Give the extent of all Trypanosoma brucei.
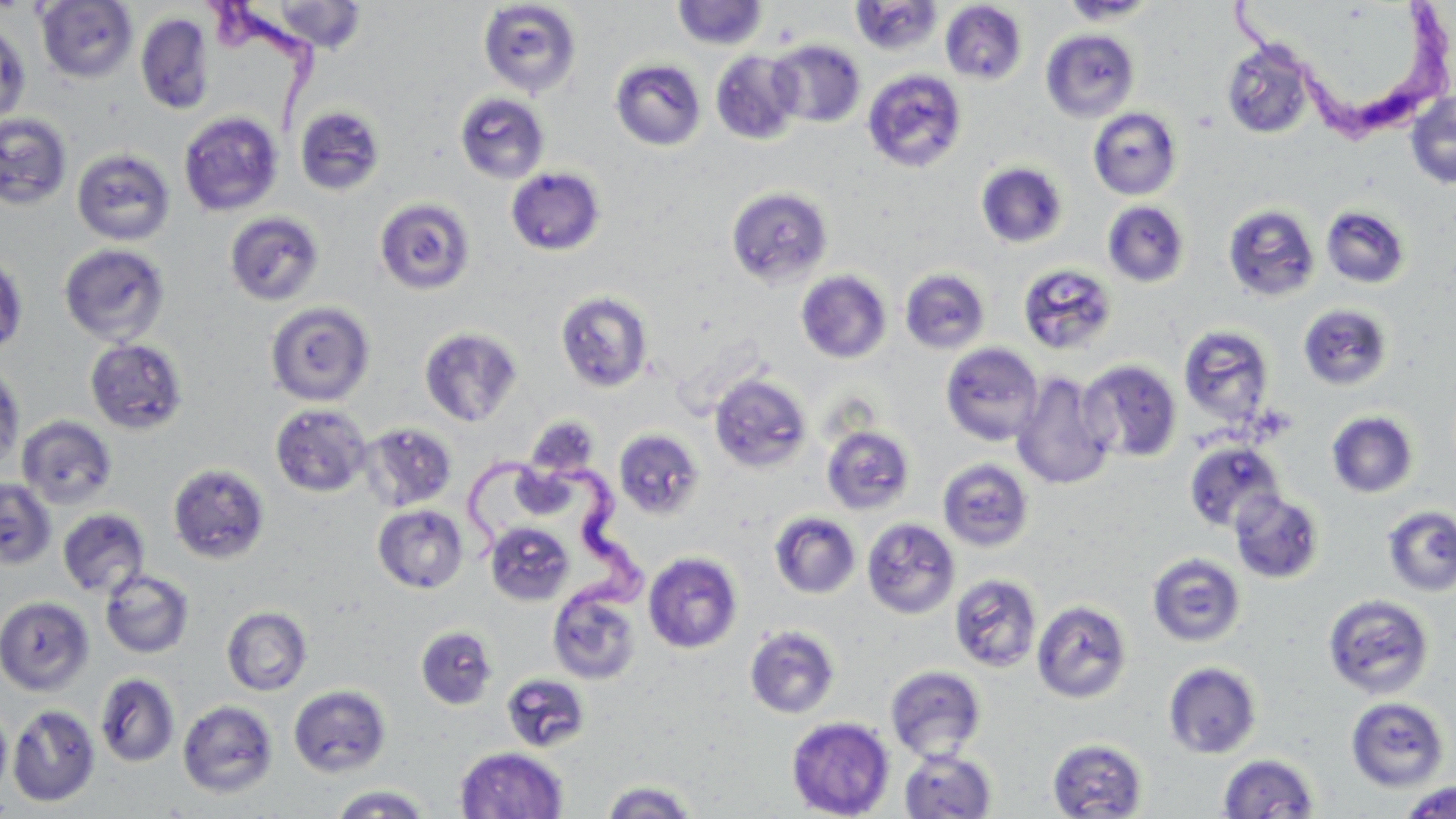

Approximate bounding boxes as named x1/y1/x2/y2 corners in pixels.
Trypanosoma brucei: (x1=202, y1=2, x2=327, y2=132), (x1=1227, y1=3, x2=1453, y2=145), (x1=457, y1=448, x2=652, y2=616).

Summary:
  - Uninfected red blood cell locations: (x1=36, y1=0, x2=138, y2=84), (x1=850, y1=0, x2=944, y2=56), (x1=1059, y1=0, x2=1161, y2=24), (x1=258, y1=1, x2=370, y2=54), (x1=478, y1=1, x2=582, y2=98), (x1=672, y1=1, x2=768, y2=50), (x1=940, y1=2, x2=1027, y2=85), (x1=135, y1=12, x2=214, y2=115), (x1=0, y1=22, x2=31, y2=126), (x1=1040, y1=28, x2=1140, y2=122), (x1=1221, y1=39, x2=1317, y2=140), (x1=768, y1=40, x2=866, y2=128), (x1=711, y1=50, x2=804, y2=145), (x1=611, y1=59, x2=706, y2=151), (x1=862, y1=68, x2=968, y2=173), (x1=1405, y1=90, x2=1456, y2=190), (x1=454, y1=92, x2=550, y2=183), (x1=294, y1=105, x2=386, y2=197), (x1=1088, y1=107, x2=1183, y2=200), (x1=178, y1=111, x2=284, y2=217), (x1=0, y1=112, x2=73, y2=211), (x1=71, y1=147, x2=176, y2=246), (x1=976, y1=162, x2=1068, y2=249), (x1=505, y1=167, x2=606, y2=256), (x1=726, y1=186, x2=833, y2=288), (x1=374, y1=197, x2=476, y2=295), (x1=1102, y1=201, x2=1191, y2=287), (x1=1222, y1=203, x2=1320, y2=302), (x1=1320, y1=205, x2=1411, y2=290), (x1=224, y1=211, x2=325, y2=306), (x1=58, y1=242, x2=171, y2=347), (x1=0, y1=251, x2=28, y2=356), (x1=1018, y1=262, x2=1118, y2=355), (x1=900, y1=268, x2=991, y2=354), (x1=796, y1=270, x2=892, y2=364), (x1=555, y1=291, x2=654, y2=393), (x1=265, y1=301, x2=375, y2=406), (x1=1297, y1=303, x2=1395, y2=391), (x1=1178, y1=324, x2=1276, y2=428), (x1=419, y1=327, x2=523, y2=427), (x1=84, y1=337, x2=189, y2=436), (x1=940, y1=342, x2=1044, y2=446), (x1=1078, y1=359, x2=1183, y2=463), (x1=0, y1=364, x2=25, y2=470), (x1=1011, y1=371, x2=1117, y2=490), (x1=709, y1=373, x2=812, y2=473), (x1=270, y1=404, x2=372, y2=496), (x1=1325, y1=410, x2=1419, y2=499), (x1=16, y1=415, x2=116, y2=509), (x1=360, y1=423, x2=457, y2=511), (x1=821, y1=425, x2=915, y2=515), (x1=613, y1=429, x2=705, y2=520), (x1=1184, y1=441, x2=1284, y2=533), (x1=937, y1=458, x2=1034, y2=552), (x1=167, y1=463, x2=271, y2=565), (x1=0, y1=478, x2=58, y2=570), (x1=1230, y1=490, x2=1325, y2=584), (x1=373, y1=504, x2=469, y2=594), (x1=1382, y1=505, x2=1456, y2=596), (x1=57, y1=508, x2=150, y2=598), (x1=770, y1=511, x2=861, y2=599), (x1=861, y1=517, x2=960, y2=619), (x1=485, y1=522, x2=575, y2=606), (x1=643, y1=551, x2=743, y2=654), (x1=1147, y1=553, x2=1246, y2=647), (x1=100, y1=569, x2=195, y2=658), (x1=949, y1=573, x2=1043, y2=673), (x1=548, y1=586, x2=642, y2=686), (x1=1322, y1=594, x2=1435, y2=699), (x1=0, y1=596, x2=95, y2=695), (x1=1032, y1=599, x2=1132, y2=704), (x1=221, y1=605, x2=312, y2=696), (x1=744, y1=624, x2=841, y2=719), (x1=415, y1=625, x2=498, y2=709), (x1=1163, y1=661, x2=1263, y2=759), (x1=885, y1=665, x2=986, y2=762), (x1=95, y1=672, x2=180, y2=767), (x1=501, y1=673, x2=591, y2=752), (x1=288, y1=684, x2=391, y2=778), (x1=1345, y1=696, x2=1450, y2=793), (x1=177, y1=700, x2=278, y2=799), (x1=0, y1=704, x2=11, y2=802), (x1=7, y1=704, x2=101, y2=807), (x1=786, y1=716, x2=895, y2=819), (x1=1047, y1=737, x2=1148, y2=819), (x1=455, y1=747, x2=568, y2=819), (x1=899, y1=748, x2=996, y2=819), (x1=1218, y1=753, x2=1320, y2=818), (x1=599, y1=780, x2=700, y2=817), (x1=1398, y1=781, x2=1456, y2=819), (x1=328, y1=784, x2=433, y2=818)
  - Slide-level diagnosis: Trypanosoma brucei
  - Image size: 1456×819 pixels
  - Preparation: thin blood film
  - Stain: May-Grünwald-Giemsa
  - Field of view: one of a larger specimen
  - Magnification: 1000x
  - Modality: optical microscopy